Classify this cell by malaria status.
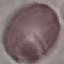
Uninfected.

{
  "image_type": "cell patch, automatically extracted from a larger field of view and resized to 64 × 64 pixels",
  "preparation": "thin blood smear",
  "capture": "smartphone camera at the microscope eyepiece",
  "stain": "Giemsa"
}